Outline each Trypanosoma brucei.
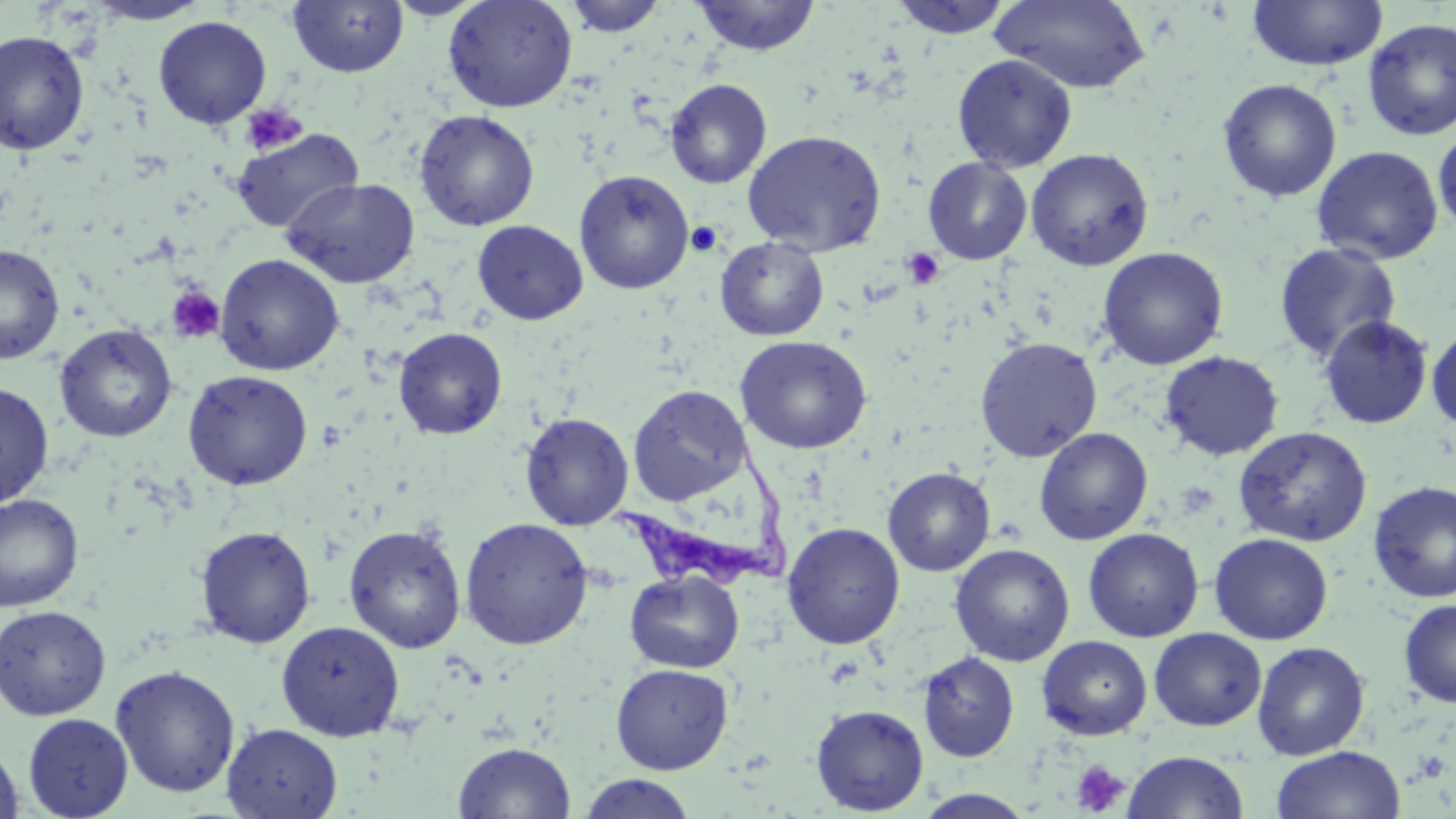
Approximate bounding boxes as (x1, y1, x2, y2) in pixels.
Trypanosoma brucei: (609, 434, 793, 588).

slide-level diagnosis = Trypanosoma brucei
modality = optical microscopy
stain = May-Grünwald-Giemsa
magnification = 1000x
platelet locations = approximate bounding boxes as (x1, y1, x2, y2) in pixels: (240, 102, 308, 156), (686, 221, 723, 257), (902, 247, 945, 290), (166, 286, 226, 344), (1175, 482, 1219, 518), (1071, 759, 1130, 816)
uninfected red blood cell locations = approximate bounding boxes as (x1, y1, x2, y2) in pixels: (385, 0, 488, 20), (443, 0, 578, 113), (564, 0, 666, 37), (691, 0, 821, 56), (888, 0, 1014, 40), (1247, 0, 1388, 71), (84, 1, 210, 26), (287, 1, 408, 77), (991, 1, 1151, 94), (153, 16, 272, 128), (1362, 17, 1456, 142), (0, 30, 90, 155), (952, 53, 1077, 173), (665, 79, 771, 189), (1217, 79, 1343, 202), (414, 109, 540, 231), (1433, 126, 1456, 233), (232, 127, 364, 233), (742, 129, 887, 256), (1311, 145, 1444, 265), (1026, 148, 1154, 270), (923, 156, 1032, 265), (573, 169, 694, 294), (282, 177, 420, 289), (472, 220, 588, 325), (716, 236, 829, 341), (1273, 242, 1402, 364), (0, 244, 65, 364), (1097, 246, 1229, 370), (214, 253, 344, 375), (1318, 315, 1433, 430), (54, 324, 177, 443), (1427, 325, 1456, 432), (393, 327, 508, 439), (734, 335, 872, 454), (975, 336, 1103, 462), (1159, 351, 1285, 461), (183, 369, 313, 490), (0, 382, 54, 508), (628, 384, 751, 506), (520, 412, 633, 530), (1234, 426, 1372, 546), (1034, 427, 1153, 545), (883, 467, 995, 577), (1368, 480, 1456, 603), (0, 493, 84, 612), (459, 517, 594, 650), (782, 522, 905, 649), (343, 523, 467, 653), (195, 525, 317, 648), (1083, 527, 1204, 642), (1209, 533, 1333, 644), (950, 544, 1075, 666), (625, 569, 745, 673), (1398, 598, 1456, 707), (0, 605, 111, 720), (276, 620, 405, 741), (1148, 627, 1266, 730), (1036, 635, 1153, 741), (1251, 640, 1371, 760), (917, 651, 1019, 762), (610, 663, 733, 774), (110, 665, 240, 798), (810, 703, 929, 815), (22, 714, 133, 818), (222, 723, 343, 819), (0, 740, 24, 819), (453, 741, 576, 819), (1271, 745, 1406, 819), (1122, 750, 1249, 818), (577, 773, 698, 818), (913, 789, 1038, 818)
field of view = single
image size = 1456×819 pixels
preparation = thin blood smear